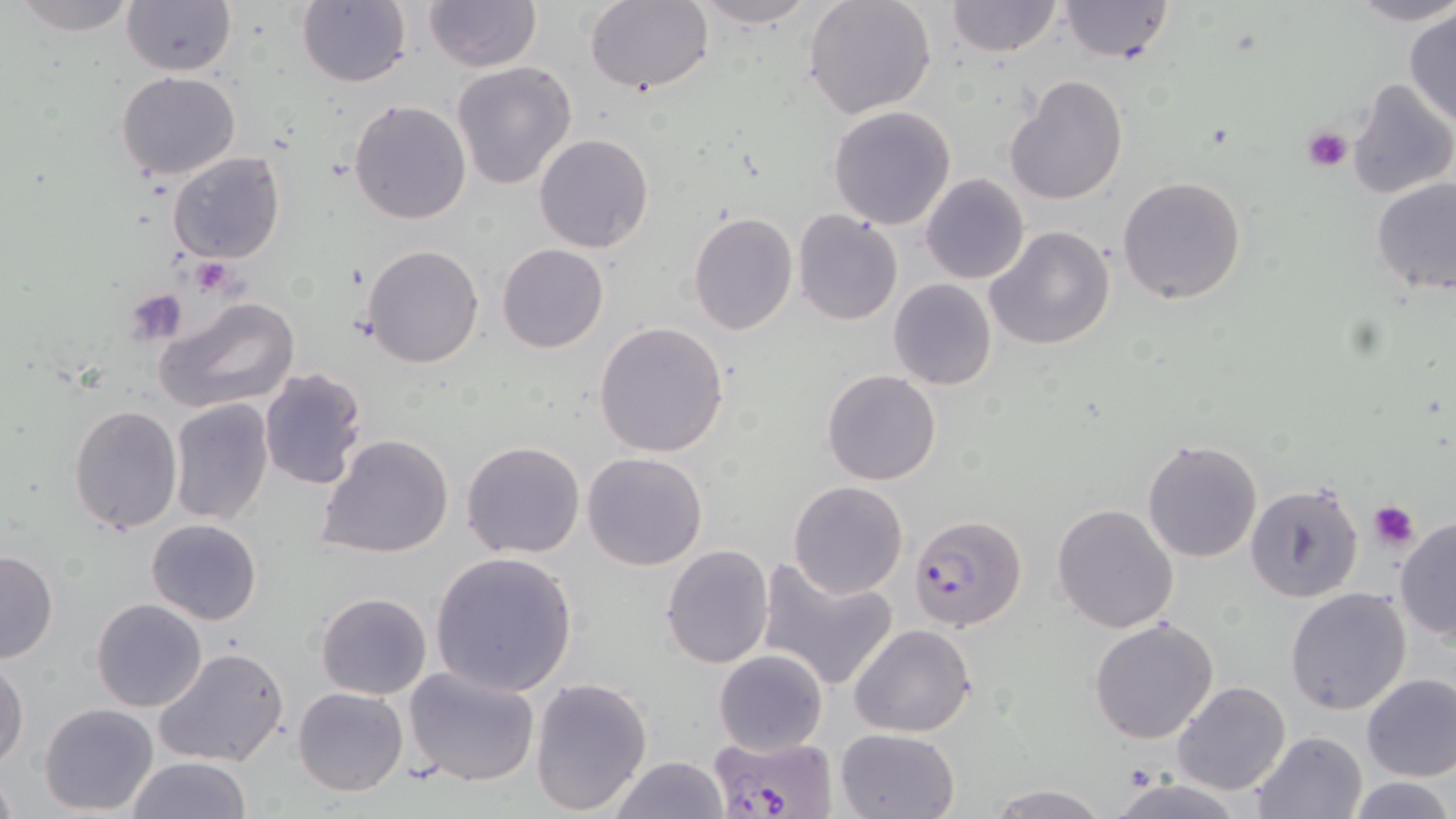

{
  "slide_level_diagnosis": "Plasmodium falciparum",
  "uninfected_red_blood_cell_locations": "approximate bounding boxes as named x1/y1/x2/y2 corners in pixels: (x1=9, y1=0, x2=139, y2=37), (x1=121, y1=0, x2=236, y2=77), (x1=689, y1=0, x2=822, y2=28), (x1=803, y1=0, x2=938, y2=118), (x1=944, y1=0, x2=1062, y2=57), (x1=1056, y1=0, x2=1175, y2=63), (x1=1346, y1=0, x2=1456, y2=26), (x1=296, y1=1, x2=412, y2=88), (x1=424, y1=1, x2=541, y2=72), (x1=584, y1=2, x2=714, y2=96), (x1=1404, y1=9, x2=1455, y2=128), (x1=452, y1=61, x2=577, y2=191), (x1=114, y1=70, x2=241, y2=180), (x1=1005, y1=75, x2=1128, y2=207), (x1=1346, y1=78, x2=1456, y2=202), (x1=348, y1=98, x2=472, y2=225), (x1=829, y1=105, x2=957, y2=229), (x1=533, y1=133, x2=654, y2=254), (x1=167, y1=151, x2=287, y2=263), (x1=920, y1=174, x2=1030, y2=286), (x1=1118, y1=175, x2=1248, y2=305), (x1=1371, y1=178, x2=1456, y2=294), (x1=687, y1=210, x2=798, y2=335), (x1=792, y1=210, x2=905, y2=328), (x1=984, y1=226, x2=1116, y2=352), (x1=360, y1=243, x2=486, y2=368), (x1=496, y1=243, x2=608, y2=353), (x1=888, y1=278, x2=996, y2=389), (x1=156, y1=295, x2=300, y2=414), (x1=593, y1=320, x2=729, y2=457), (x1=258, y1=367, x2=368, y2=491), (x1=822, y1=369, x2=942, y2=486), (x1=168, y1=398, x2=275, y2=525), (x1=66, y1=404, x2=182, y2=534), (x1=316, y1=433, x2=454, y2=560), (x1=1141, y1=438, x2=1264, y2=563), (x1=461, y1=440, x2=585, y2=559), (x1=582, y1=451, x2=709, y2=570), (x1=788, y1=481, x2=908, y2=598), (x1=1243, y1=481, x2=1364, y2=604), (x1=1052, y1=503, x2=1179, y2=634), (x1=1394, y1=516, x2=1456, y2=642), (x1=146, y1=519, x2=263, y2=626), (x1=661, y1=543, x2=775, y2=667), (x1=0, y1=549, x2=58, y2=664), (x1=427, y1=551, x2=579, y2=697), (x1=757, y1=556, x2=900, y2=692), (x1=1284, y1=587, x2=1412, y2=717), (x1=316, y1=591, x2=432, y2=700), (x1=91, y1=598, x2=207, y2=713), (x1=1089, y1=615, x2=1220, y2=744), (x1=848, y1=623, x2=977, y2=737), (x1=153, y1=646, x2=291, y2=768), (x1=714, y1=649, x2=829, y2=754), (x1=1, y1=660, x2=27, y2=768), (x1=403, y1=665, x2=543, y2=789), (x1=1361, y1=672, x2=1456, y2=782), (x1=530, y1=676, x2=653, y2=814), (x1=1172, y1=681, x2=1291, y2=797), (x1=292, y1=686, x2=408, y2=796), (x1=40, y1=703, x2=160, y2=815), (x1=835, y1=727, x2=959, y2=819), (x1=1245, y1=731, x2=1368, y2=819), (x1=610, y1=755, x2=729, y2=819), (x1=127, y1=756, x2=253, y2=818), (x1=0, y1=770, x2=19, y2=818), (x1=1104, y1=776, x2=1251, y2=819), (x1=1345, y1=776, x2=1453, y2=818), (x1=985, y1=783, x2=1108, y2=818)",
  "magnification": "1000x",
  "modality": "optical microscopy",
  "plasmodium_falciparum_infected_red_blood_cell_locations": "approximate bounding boxes as named x1/y1/x2/y2 corners in pixels: (x1=909, y1=513, x2=1028, y2=630), (x1=705, y1=733, x2=841, y2=819)",
  "preparation": "thin blood smear",
  "field_of_view": "single",
  "stain": "May-Grünwald-Giemsa",
  "image_size": "1456×819 pixels",
  "platelet_locations": "approximate bounding boxes as named x1/y1/x2/y2 corners in pixels: (x1=1301, y1=125, x2=1352, y2=173), (x1=189, y1=259, x2=237, y2=297), (x1=123, y1=289, x2=188, y2=346), (x1=1369, y1=501, x2=1420, y2=551)"
}